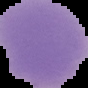
image_type: cell region segmented out of the field of view; surrounding area masked to black
image_size: 88×88 pixels
preparation: thin blood smear
malaria_status: uninfected